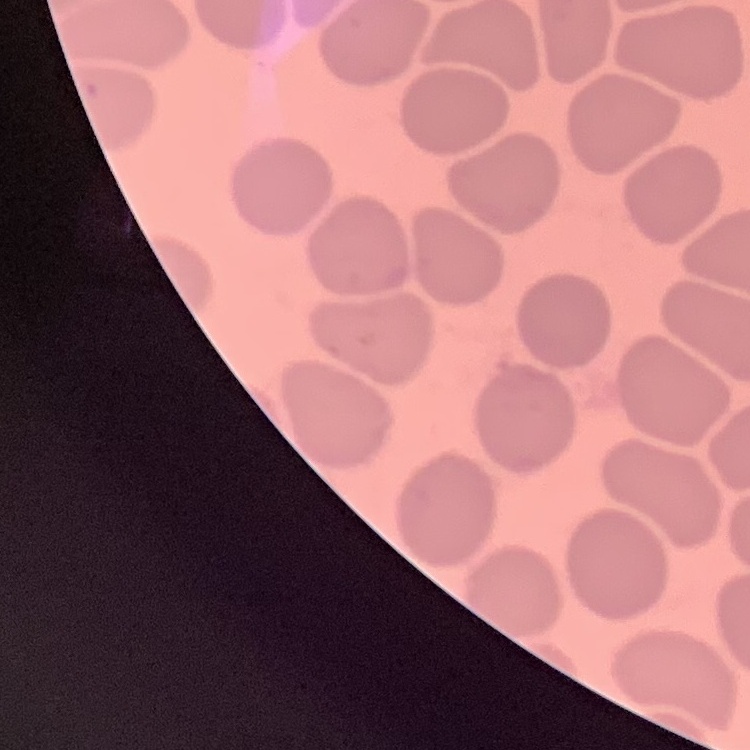
The erythrocytes exhibit no rouleaux formation. Thin blood film. One tile cut from a larger photomicrograph. Stained with either Field's or Giemsa.